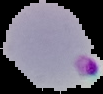
Summary:
  - Image size: 103×94 pixels
  - Preparation: thin blood film
  - Malaria status: parasitized
  - Image type: segmented cell region on a black background